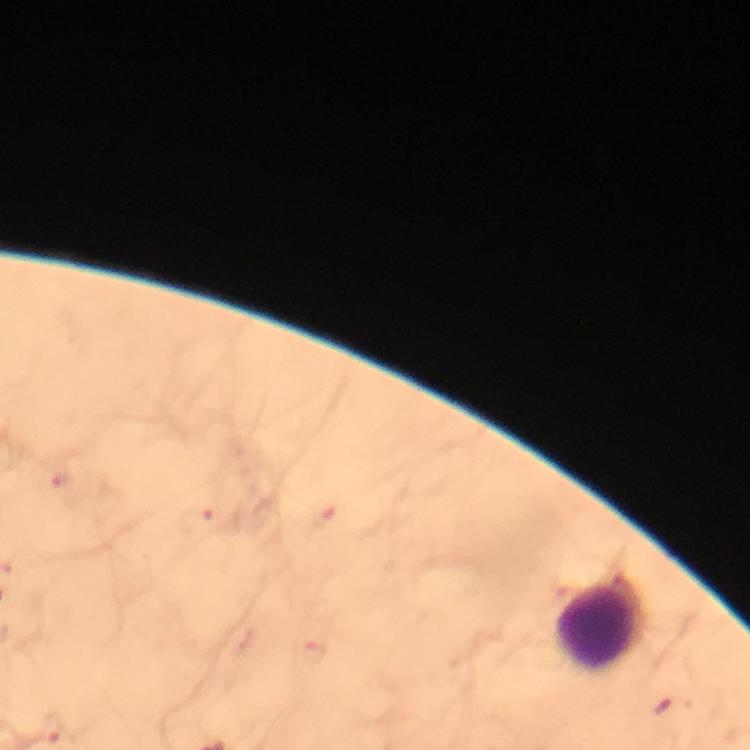
Approximate centers as {x, y} in pixels. Leukocyte locations: {597, 626}. Malaria parasite locations: {198, 520}, {315, 651}, {665, 709}, {55, 728}. Image is 750×750 pixels. From a malaria diagnostic workup. At 100x magnification. Immersion oil applied. Photographed with a smartphone mounted on the microscope. Giemsa-stained preparation. Thick smear. Cropped region of a single field of view.